Identify the cell.
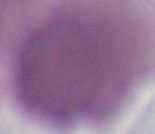
This is an erythrocyte.

Summary:
  - Magnification: 1000x
  - Modality: photomicrograph